Assess this cell for malaria.
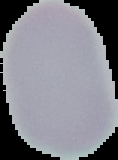

It is uninfected.

Summary:
  - Image type: segmented cell region with the area outside set to black
  - Image size: 118×160 pixels
  - Preparation: thin blood smear